Classify this cell by malaria status.
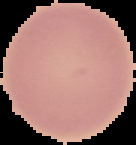
It is uninfected.

image type = segmented cell region with the area outside set to black
preparation = thin blood film
image size = 136×145 pixels